Identify the cell.
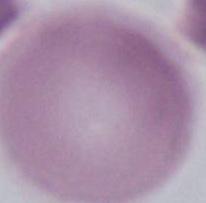

This is an erythrocyte.

Photomicrograph. Captured at 1000x magnification.